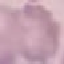 Result: no malaria parasites detected. Thin blood film. Giemsa-stained preparation. Cell patch, automatically extracted from a larger field of view and resized to 64 × 64 pixels. Photographed with a smartphone camera at the microscope eyepiece.